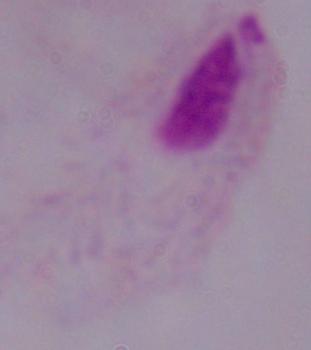

{
  "magnification": "1000x",
  "modality": "micrograph",
  "identification": "trichomonad"
}